Comment on the morphology of the red blood cells.
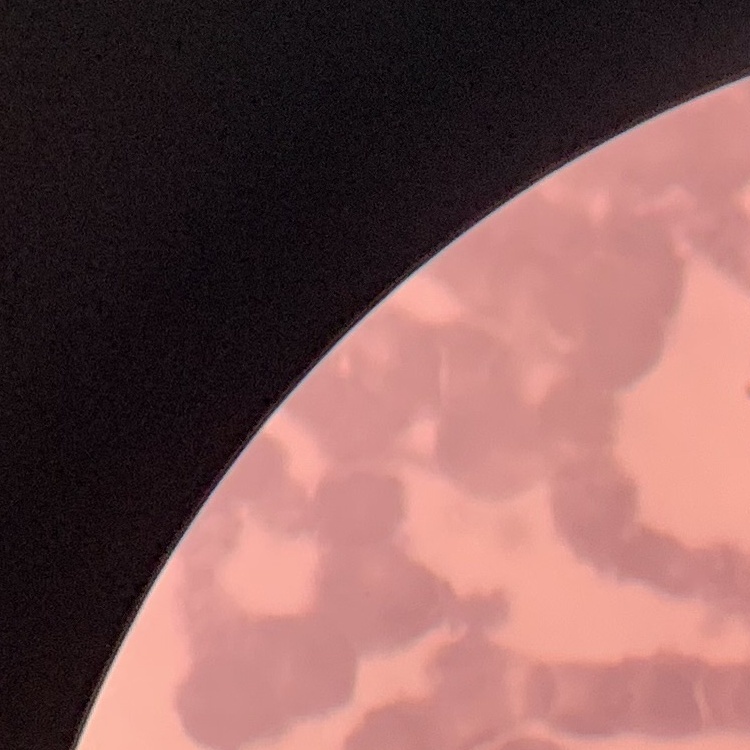
Rouleaux formation.

{
  "stain": "Field's or Giemsa",
  "image_type": "one tile cut from a larger photomicrograph",
  "preparation": "thin peripheral smear"
}